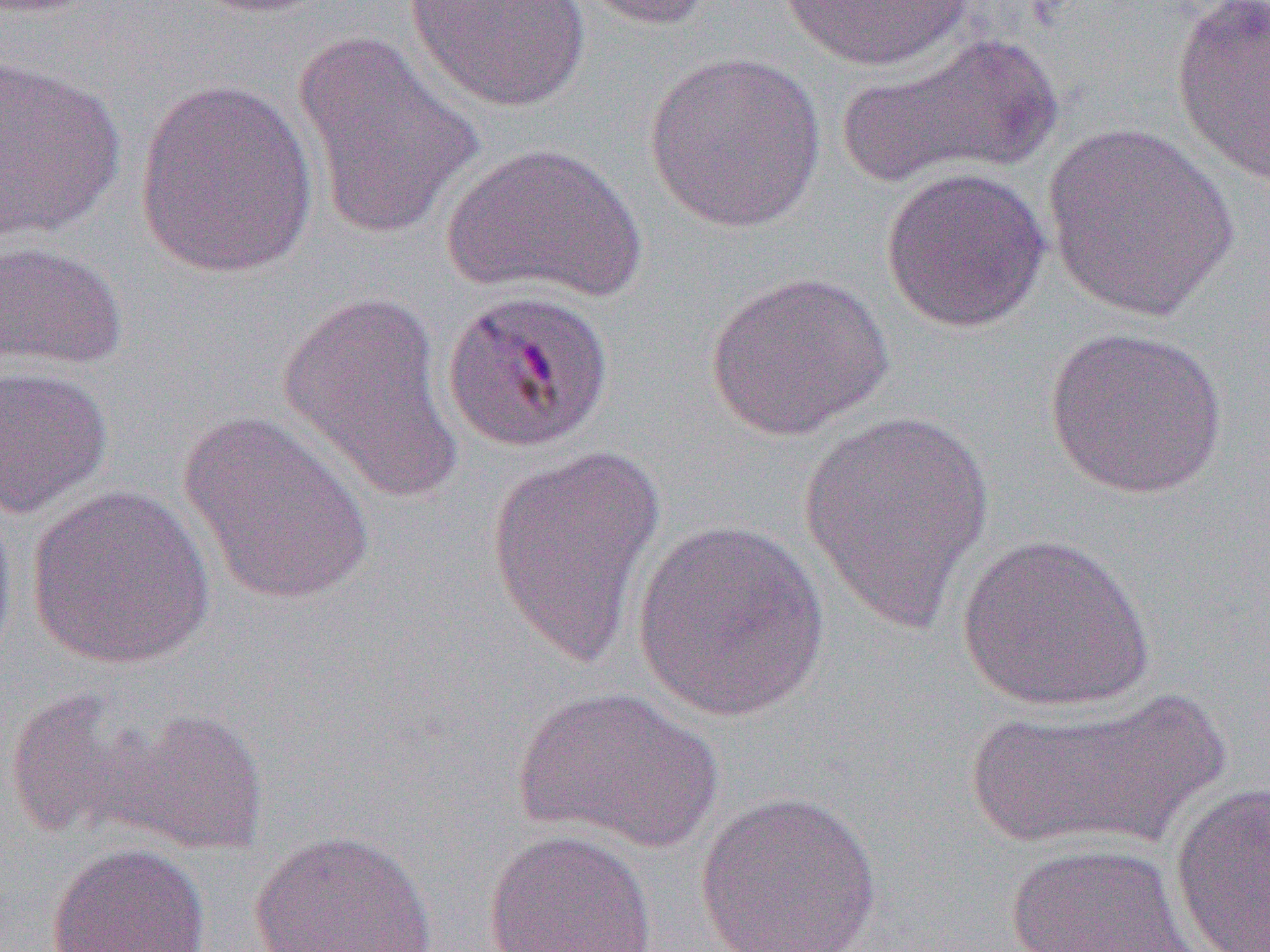

Approximate bounding boxes as (x1, y1, x2, y2) in pixels. Uninfected red blood cell locations: (187, 0, 340, 17), (403, 0, 592, 113), (574, 0, 718, 31), (777, 1, 981, 72), (1170, 1, 1270, 187), (290, 29, 485, 243), (837, 31, 1064, 188), (643, 50, 827, 233), (1, 55, 126, 242), (133, 77, 321, 279), (1041, 121, 1240, 324), (439, 141, 647, 303), (879, 165, 1051, 333), (0, 239, 127, 371), (704, 270, 894, 442), (277, 289, 463, 503), (1043, 325, 1228, 499), (0, 365, 113, 518), (178, 409, 377, 608), (797, 412, 998, 634), (485, 444, 668, 669), (25, 485, 216, 670), (0, 495, 18, 669), (632, 519, 830, 722), (957, 533, 1155, 713), (511, 685, 723, 852), (957, 685, 1235, 855), (3, 688, 152, 842), (106, 707, 270, 855), (1169, 779, 1270, 952), (692, 789, 884, 952), (248, 827, 437, 952), (482, 827, 657, 952), (45, 841, 212, 951), (1001, 841, 1204, 952). Slide-level diagnosis: Plasmodium malariae. Single field of view. Thin blood film. Optical microscopy. Image is 1270×952 pixels. Captured at 1000x magnification.